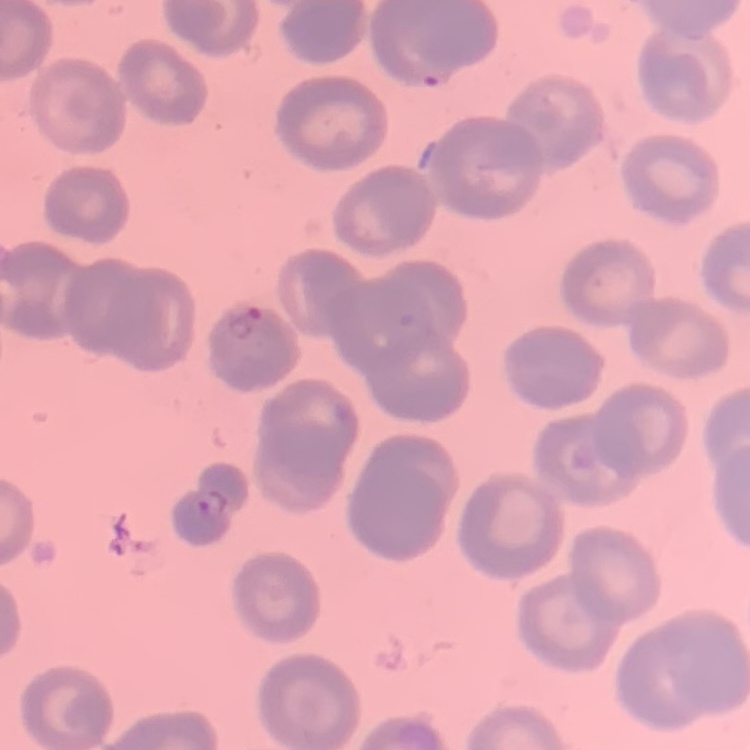
red blood cell morphology = no rouleaux formation
preparation = thin blood smear
stain = Field's or Giemsa
image type = one tile cut from a larger photomicrograph